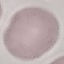

Summary:
  - Result: no malaria parasites detected
  - Preparation: thin smear
  - Capture: smartphone through the microscope eyepiece
  - Image type: cell patch, automatically extracted from a larger field of view and resized to 64 × 64 pixels
  - Stain: Giemsa